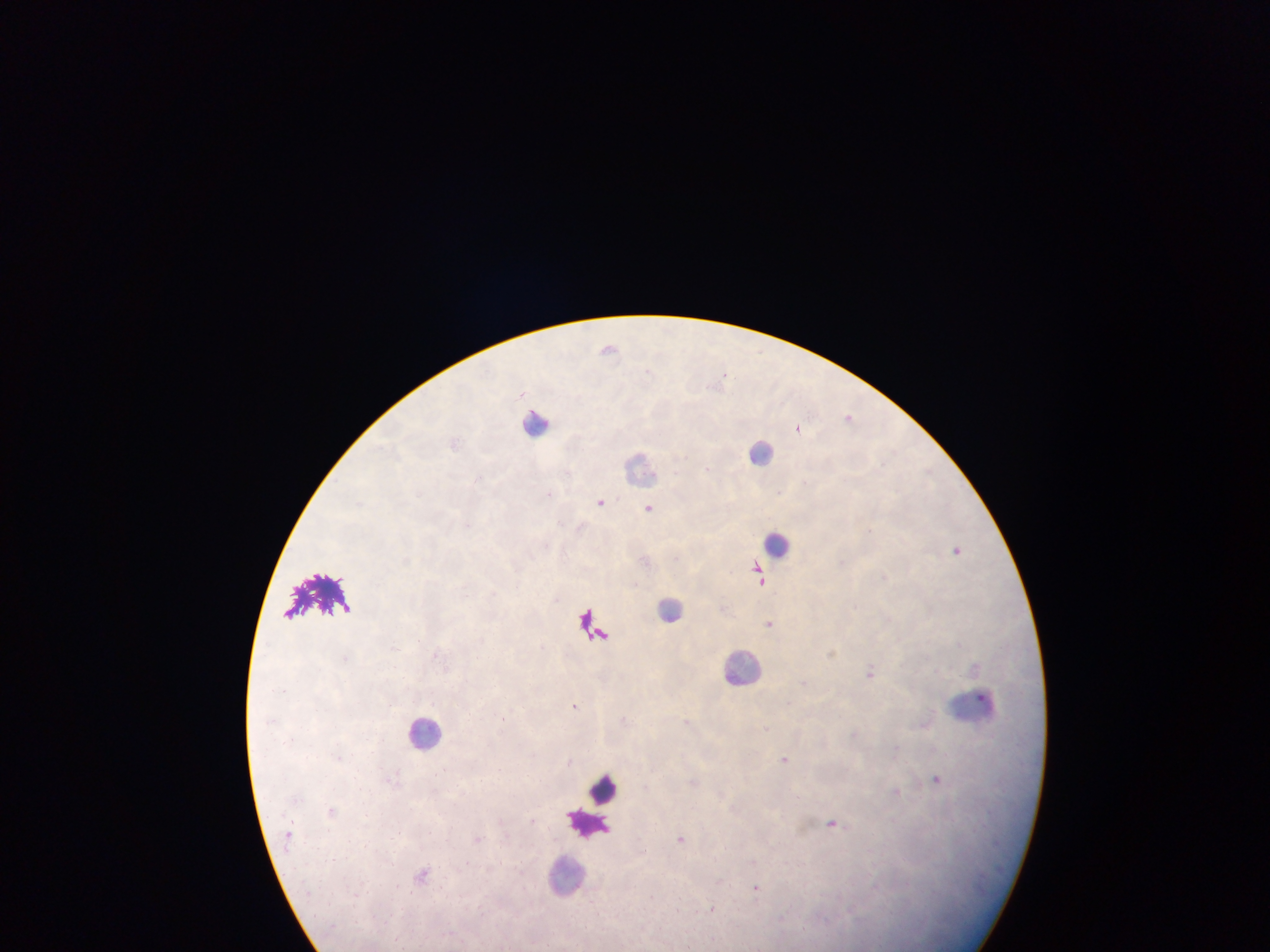 Approximate centers as x y in pixels. Leukocyte locations: 539 421; 761 452; 640 467; 777 544; 671 609; 742 666; 977 706; 427 731; 605 790; 587 823; 565 875. Plasmodium parasite locations: 608 347; 725 376; 849 416; 798 428; 708 468; 549 493; 600 502; 649 507; 869 530; 957 550; 759 576; 884 576; 769 623; 395 647; 870 671; 575 705; 784 759; 936 779; 896 792; 833 823; 681 839; 756 887; 713 907; 713 940. Collected in Ghana. Thick blood smear. One field of view. Image is 1270×952 pixels. Mobile-phone photograph taken through the microscope.